Report the malaria status of this cell.
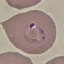
Parasitized.

Summary:
  - Image type: automatically extracted cell patch, resized to 64 × 64 pixels
  - Preparation: thin blood smear
  - Stain: Giemsa
  - Capture: smartphone through the microscope eyepiece